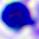

Summary:
  - Identification: leukocyte
  - Magnification: 400x
  - Modality: micrograph